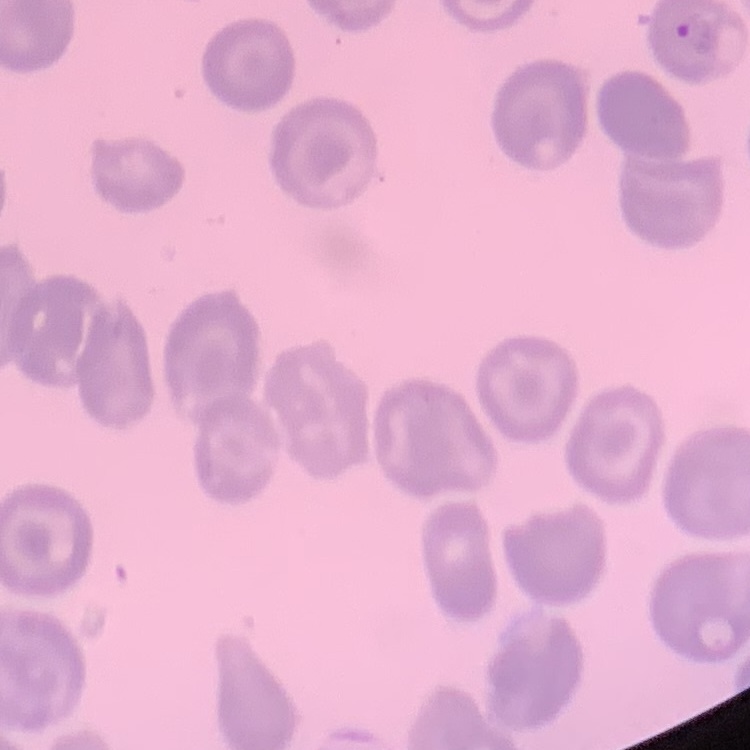
Summary:
  - Erythrocyte morphology: no rouleaux formation
  - Preparation: thin peripheral smear
  - Stain: Field's or Giemsa
  - Image type: square crop of a larger photomicrograph